Assess the morphology of the erythrocytes.
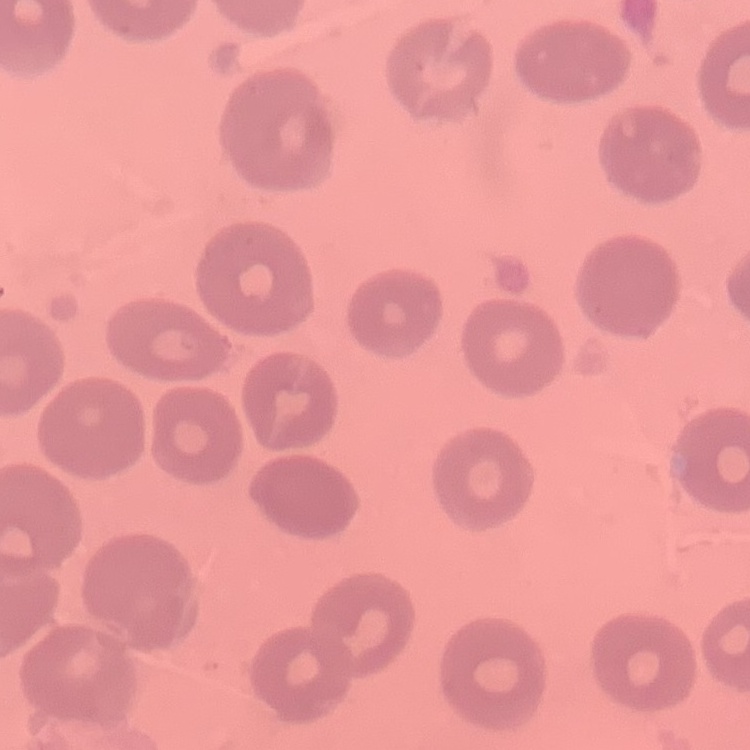
No rouleaux formation.

Summary:
  - Preparation: thin peripheral smear
  - Stain: Field's or Giemsa
  - Image type: square crop of a larger photomicrograph